Describe the morphology of the erythrocytes.
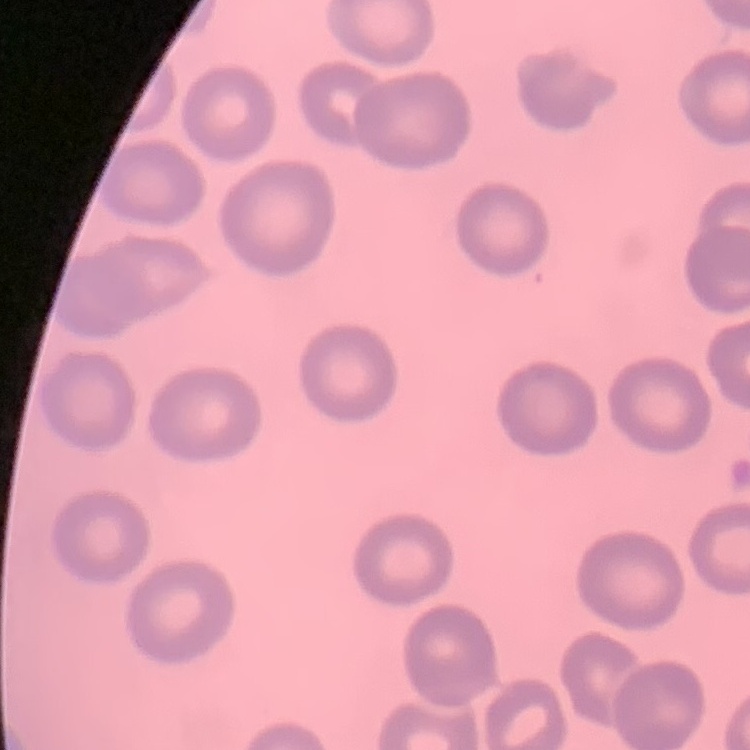
They show no rouleaux formation.

Summary:
  - Preparation: thin peripheral smear
  - Image type: one tile cut from a larger photomicrograph
  - Stain: Field's or Giemsa